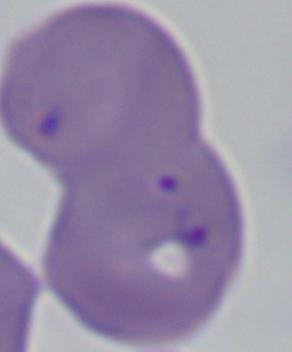

Summary:
  - Identification: Babesia
  - Magnification: 1000x
  - Modality: photomicrograph